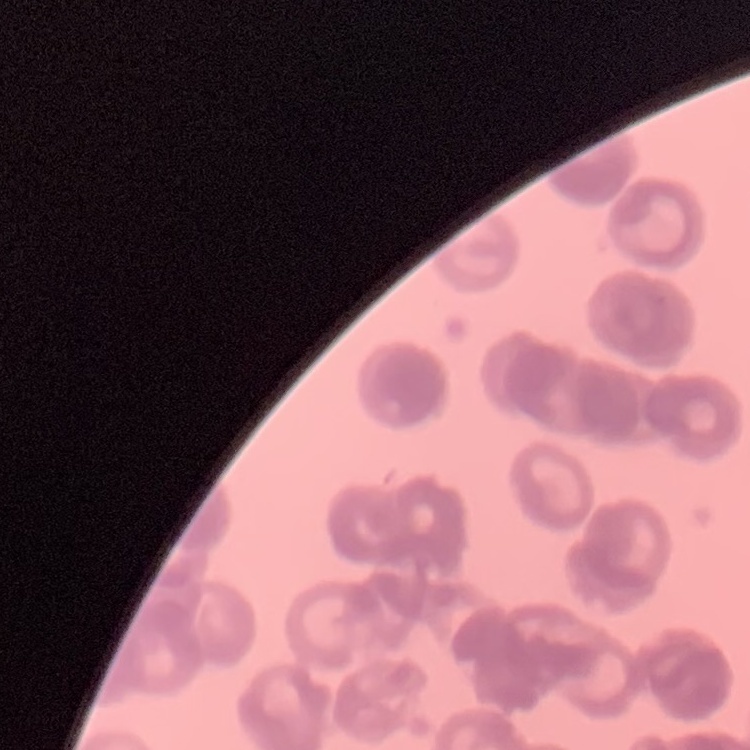
Summary:
  - Erythrocyte morphology: rouleaux formation
  - Stain: Field's or Giemsa
  - Image type: square crop of a larger photomicrograph
  - Preparation: thin peripheral smear